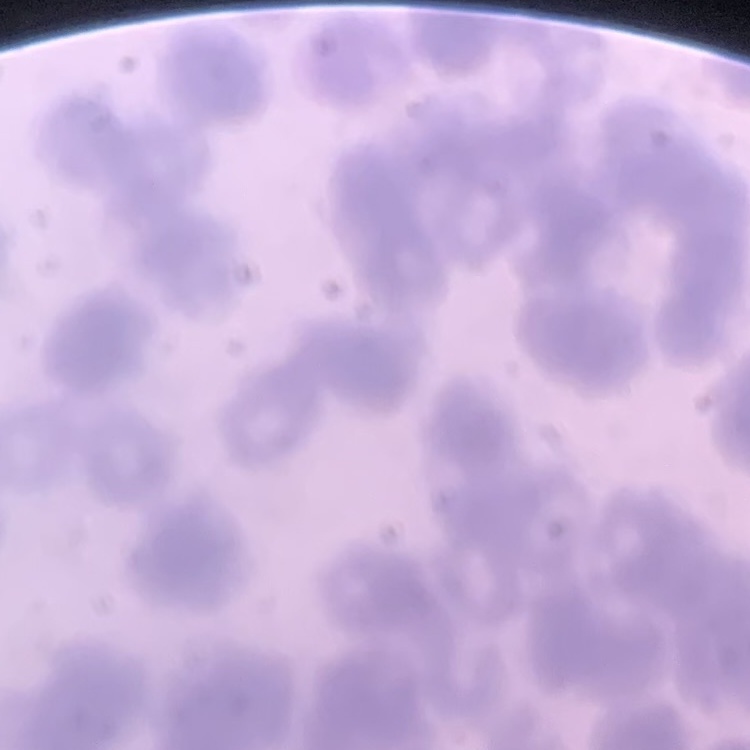

red_blood_cell_morphology: rouleaux formation
stain: Field's or Giemsa
preparation: thin blood film
image_type: square crop of a larger photomicrograph